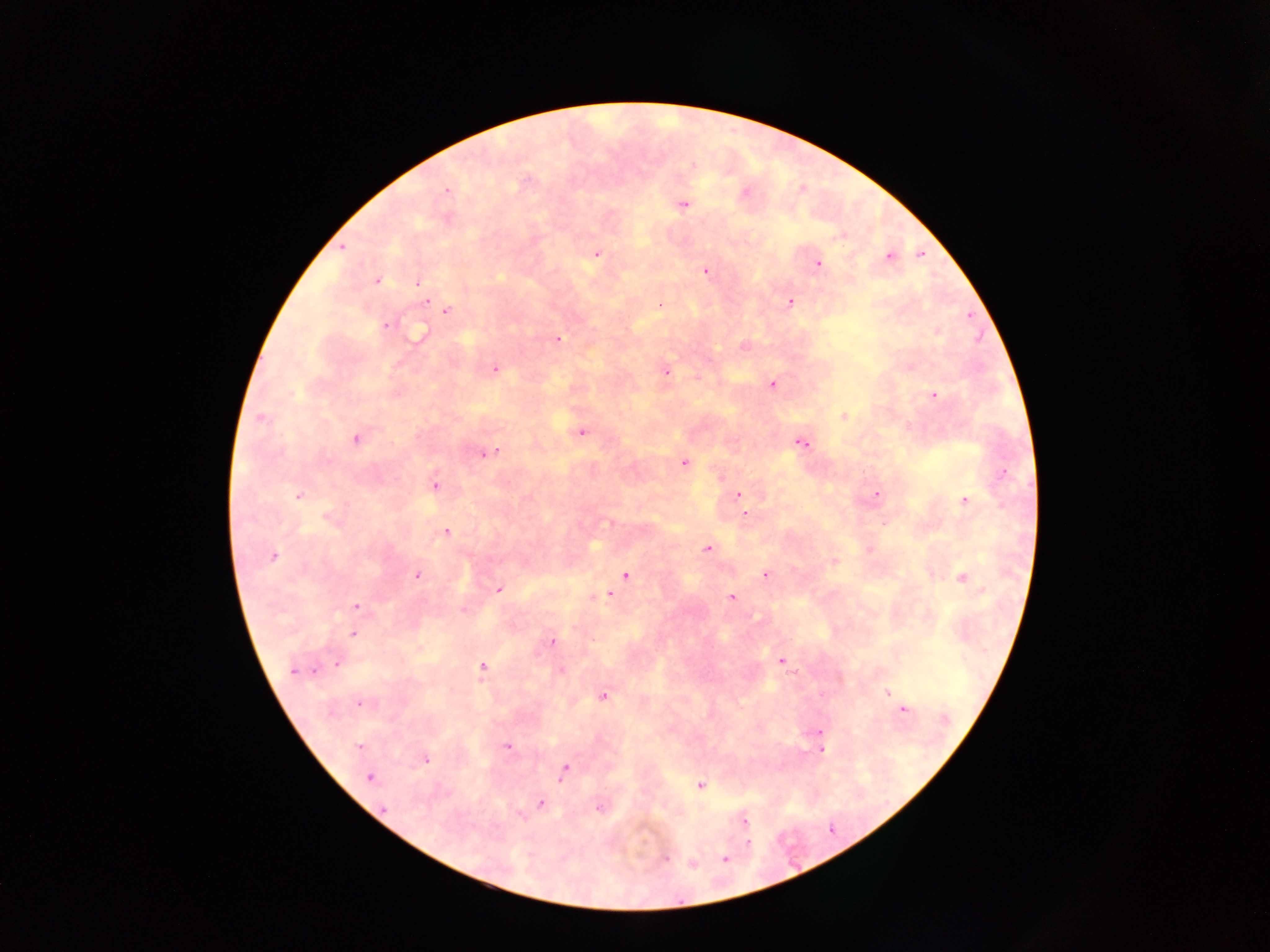
{
  "image_size": "1270×952 pixels",
  "capture": "mobile-phone photograph through a microscope",
  "plasmodium_parasite_locations": "approximate centers as (x, y) in pixels: (446, 191), (745, 192), (684, 205), (597, 254), (889, 257), (818, 263), (705, 271), (377, 280), (419, 283), (426, 302), (790, 302), (447, 310), (385, 326), (420, 333), (558, 340), (744, 347), (495, 369), (666, 371), (772, 384), (934, 394), (843, 415), (261, 419), (581, 432), (356, 438), (801, 443), (488, 453), (685, 463), (435, 484), (876, 493), (738, 494), (299, 496), (965, 499), (745, 515), (329, 519), (609, 522), (446, 532), (707, 549), (273, 556), (765, 574), (418, 575), (625, 575), (962, 578), (499, 590), (608, 596), (731, 596), (356, 606), (463, 610), (352, 634), (552, 641), (781, 660), (337, 664), (482, 667), (314, 670), (292, 671), (561, 671), (888, 692), (603, 696), (360, 704), (903, 709), (820, 732), (358, 745), (507, 746), (822, 748), (426, 760), (565, 770), (369, 777), (700, 785), (541, 803), (600, 808), (383, 809), (745, 822), (749, 843), (665, 858), (725, 859), (693, 864)",
  "preparation": "thick blood film",
  "field_of_view": "single",
  "country": "Ghana"
}